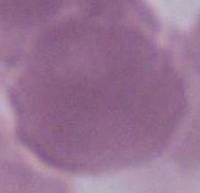

Summary:
  - Identification: red blood cell
  - Modality: micrograph
  - Magnification: 1000x